Locate every blood parasite and identify its species.
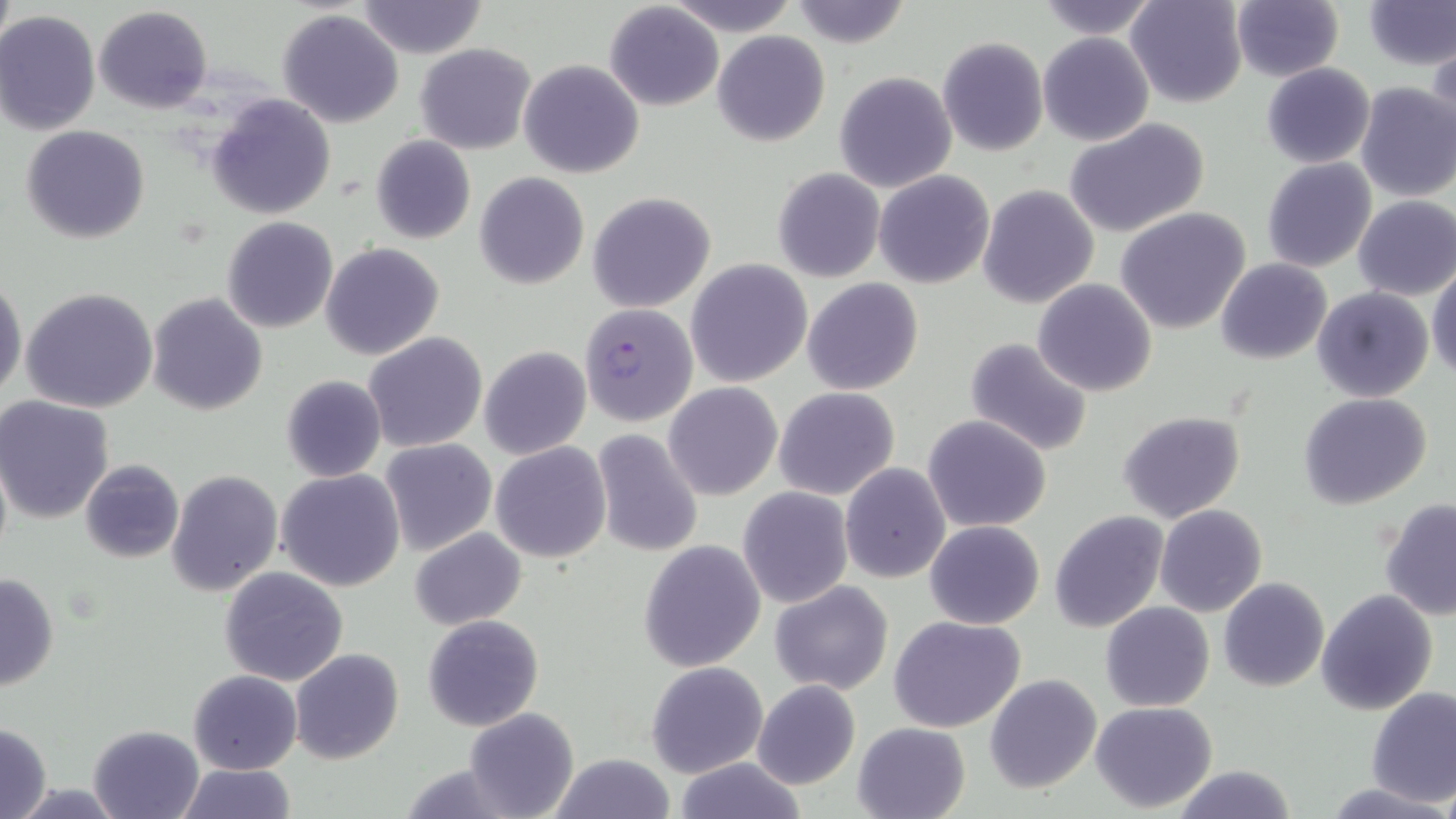

Approximate bounding boxes as [x1, y1, x2, y2] in pixels.
Plasmodium falciparum-infected red blood cells: [579, 303, 698, 427].
No Plasmodium ovale, Plasmodium malariae, Plasmodium vivax, Babesia divergens, or Trypanosoma brucei observed.

slide_level_diagnosis: Plasmodium falciparum
modality: optical microscopy
magnification: 1000x
stain: May-Grünwald-Giemsa
field_of_view: one of a larger specimen
uninfected_red_blood_cell_locations: 'approximate bounding boxes as [x1, y1, x2, y2] in pixels: [665, 0, 799, 35], [790, 0, 912, 49], [1035, 0, 1161, 40], [1126, 0, 1248, 108], [1230, 0, 1343, 82], [1362, 0, 1455, 69], [356, 1, 489, 58], [1, 2, 17, 63], [605, 2, 722, 112], [94, 5, 212, 113], [277, 8, 405, 128], [0, 9, 101, 135], [713, 30, 829, 145], [1039, 32, 1154, 147], [1428, 36, 1455, 144], [937, 37, 1048, 156], [1049, 37, 1174, 231], [415, 43, 537, 155], [519, 59, 644, 179], [1261, 63, 1375, 168], [834, 71, 957, 193], [1354, 82, 1456, 201], [208, 94, 335, 219], [1065, 119, 1211, 238], [20, 125, 150, 244], [370, 135, 475, 244], [1262, 157, 1376, 272], [772, 168, 886, 283], [874, 170, 995, 289], [474, 172, 588, 289], [977, 184, 1099, 310], [587, 191, 717, 313], [1353, 195, 1456, 300], [1117, 207, 1251, 333], [221, 217, 338, 332], [321, 242, 443, 359], [1216, 258, 1332, 365], [686, 259, 813, 388], [1429, 264, 1456, 382], [0, 275, 25, 404], [803, 278, 924, 396], [1032, 279, 1157, 398], [20, 286, 159, 414], [1312, 287, 1433, 401], [148, 293, 268, 414], [364, 332, 488, 454], [965, 337, 1093, 457], [479, 346, 591, 460], [280, 374, 387, 482], [663, 382, 782, 499], [773, 386, 901, 500], [1299, 392, 1432, 508], [2, 395, 116, 523], [1118, 411, 1246, 524], [923, 414, 1053, 532], [592, 430, 704, 556], [380, 439, 497, 555], [491, 442, 610, 564], [80, 459, 184, 564], [840, 463, 950, 583], [278, 467, 404, 592], [166, 469, 283, 596], [738, 486, 853, 608], [1379, 499, 1455, 621], [1155, 505, 1267, 617], [1050, 511, 1168, 633], [925, 520, 1045, 630], [410, 527, 526, 630], [638, 540, 766, 671], [219, 565, 349, 685], [0, 573, 59, 691], [1219, 577, 1329, 691], [770, 580, 894, 695], [1315, 590, 1436, 714], [1101, 601, 1215, 711], [423, 614, 543, 730], [889, 615, 1026, 733], [290, 648, 405, 765], [645, 661, 768, 778], [189, 669, 302, 775], [984, 674, 1102, 793], [752, 680, 861, 789], [1366, 688, 1456, 807], [1090, 701, 1218, 813], [463, 706, 578, 818], [852, 721, 971, 819], [0, 723, 52, 819], [87, 723, 206, 818], [547, 754, 679, 818], [672, 757, 808, 818], [174, 763, 297, 819], [1170, 765, 1298, 819], [1331, 781, 1449, 816]'
image_size: 1456×819 pixels
preparation: thin blood smear